Classify this cell by malaria status.
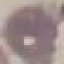

It is uninfected.

preparation = thin smear
image type = cell patch, automatically extracted from a larger field of view and resized to 64 × 64 pixels
capture = smartphone camera at the microscope eyepiece
stain = Giemsa